Evaluate for parasitized red blood cells.
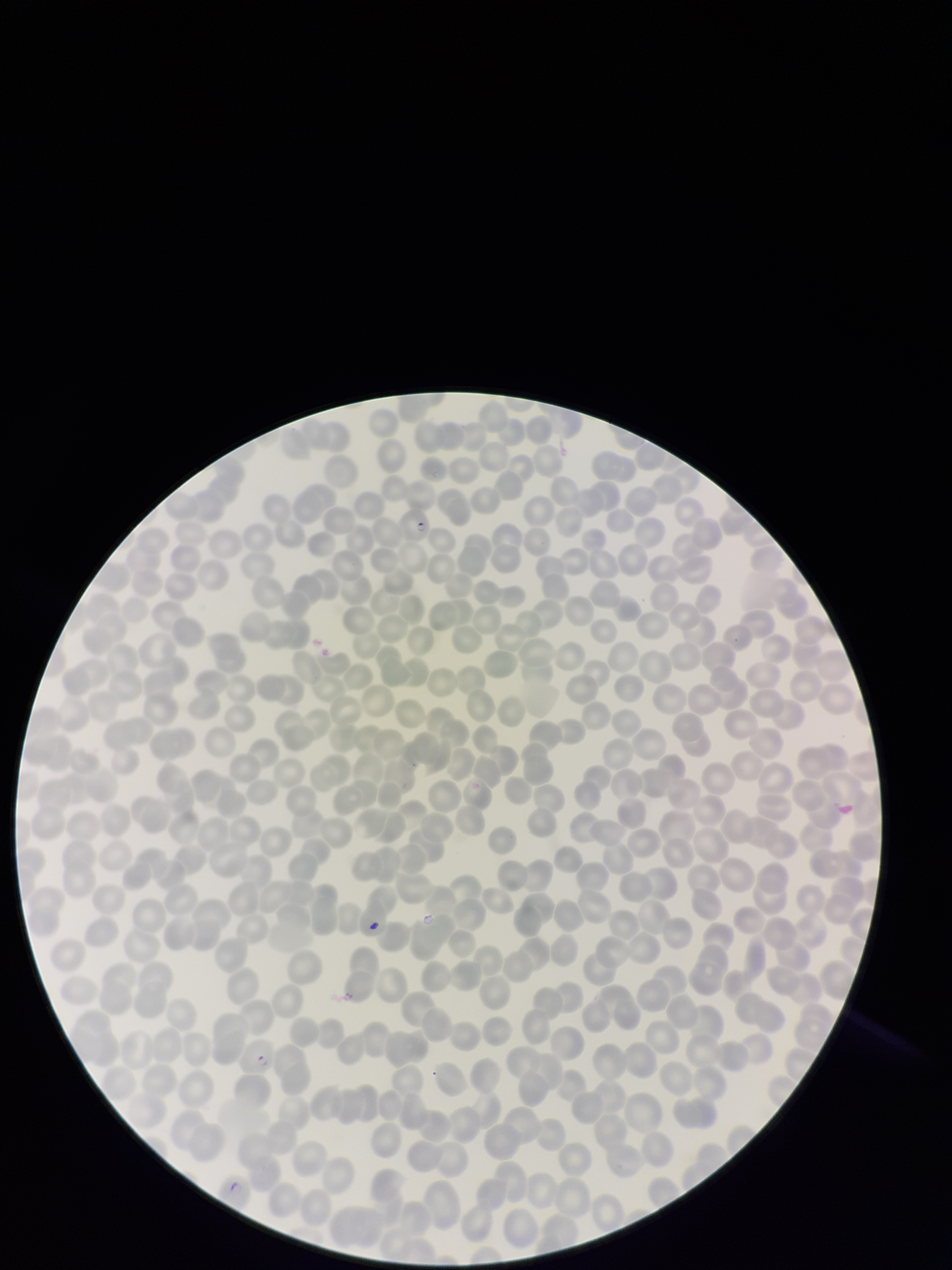

Detected.

Summary:
  - Species reported for this patient: Plasmodium falciparum
  - Parasitized red blood cell count: 2
  - Field of view: one from this slide
  - Image size: 952×1270 pixels
  - Stain: Giemsa
  - Red blood cell count: 369
  - Preparation: thin blood smear
  - Patient malaria status: infected
  - Capture: smartphone photograph through the microscope eyepiece